Describe the morphology of the erythrocytes.
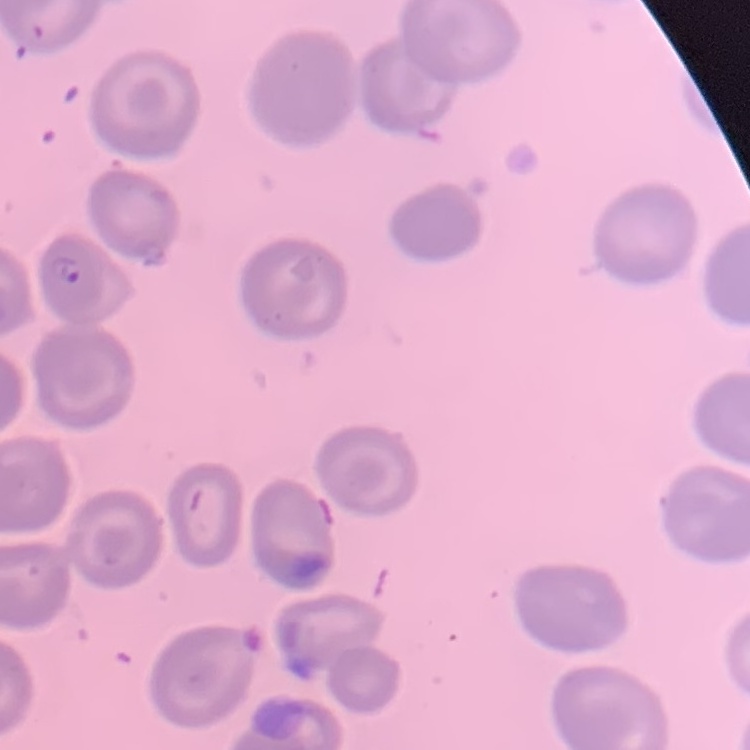

They show no rouleaux formation.

preparation = thin blood film
stain = Field's or Giemsa
image type = square crop of a larger photomicrograph